Describe the morphology of the erythrocytes.
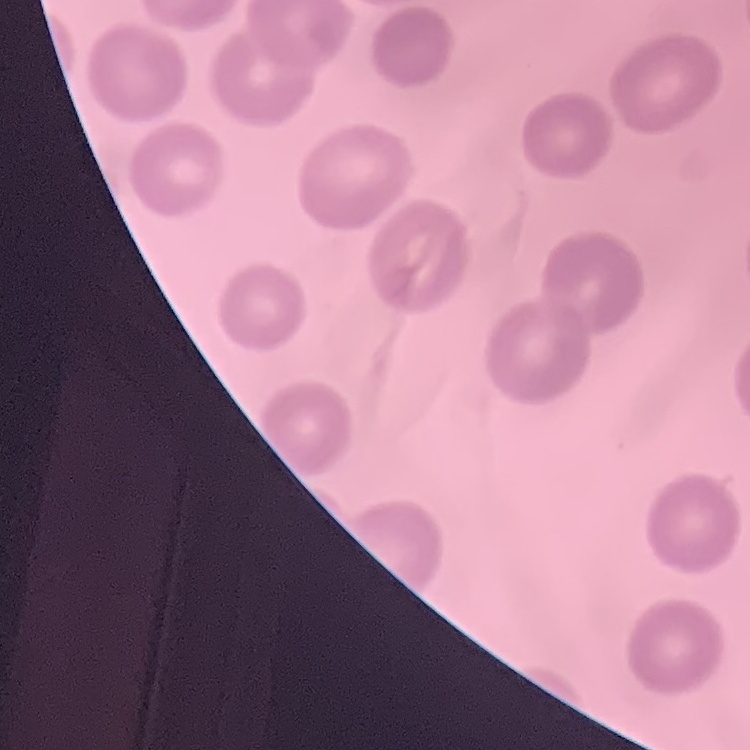
No rouleaux formation.

image type = square crop of a larger photomicrograph
preparation = thin peripheral smear
stain = Field's or Giemsa